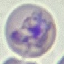
Result: malaria parasites identified. Acquired by smartphone through the microscope eyepiece. Giemsa-stained preparation. Automatically extracted cell patch, resized to 64 × 64 pixels. Thin blood smear.